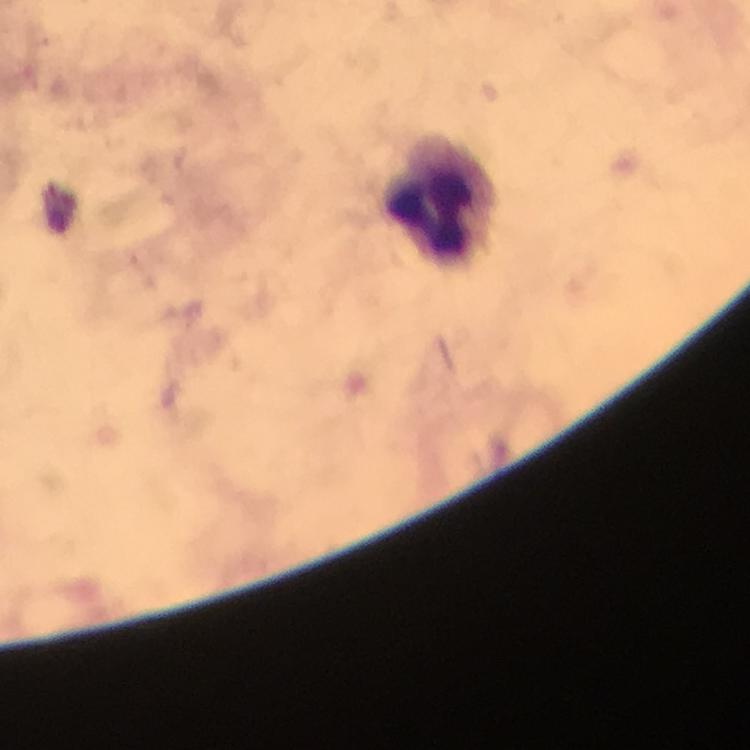

Approximate centers as {x, y} in pixels. Leukocyte locations: {442, 198}. A crop from one field of view. Giemsa stain. From a malaria diagnostic workup. 100x magnification. Plasmodium parasites: none detected. Thick blood smear. Image is 750×750 pixels. Immersion oil applied. Photographed with a smartphone mounted on the microscope.